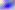
Micrograph. Toxoplasma gondii is seen. 400x magnification.